Report the malaria status of this cell.
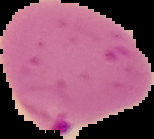

Parasitized.

Summary:
  - Preparation: thin blood film
  - Image size: 154×139 pixels
  - Image type: cell region segmented out of the field of view; surrounding area masked to black